Assess this cell for malaria.
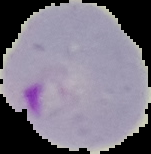
It is parasitized.

preparation: thin blood smear
image_type: segmented cell region on a black background
image_size: 151×154 pixels